Classify this cell by malaria status.
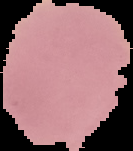
Uninfected.

From a thin blood film. Cell region segmented out of the field of view; the surrounding area is masked to black. Image is 133×151 pixels.